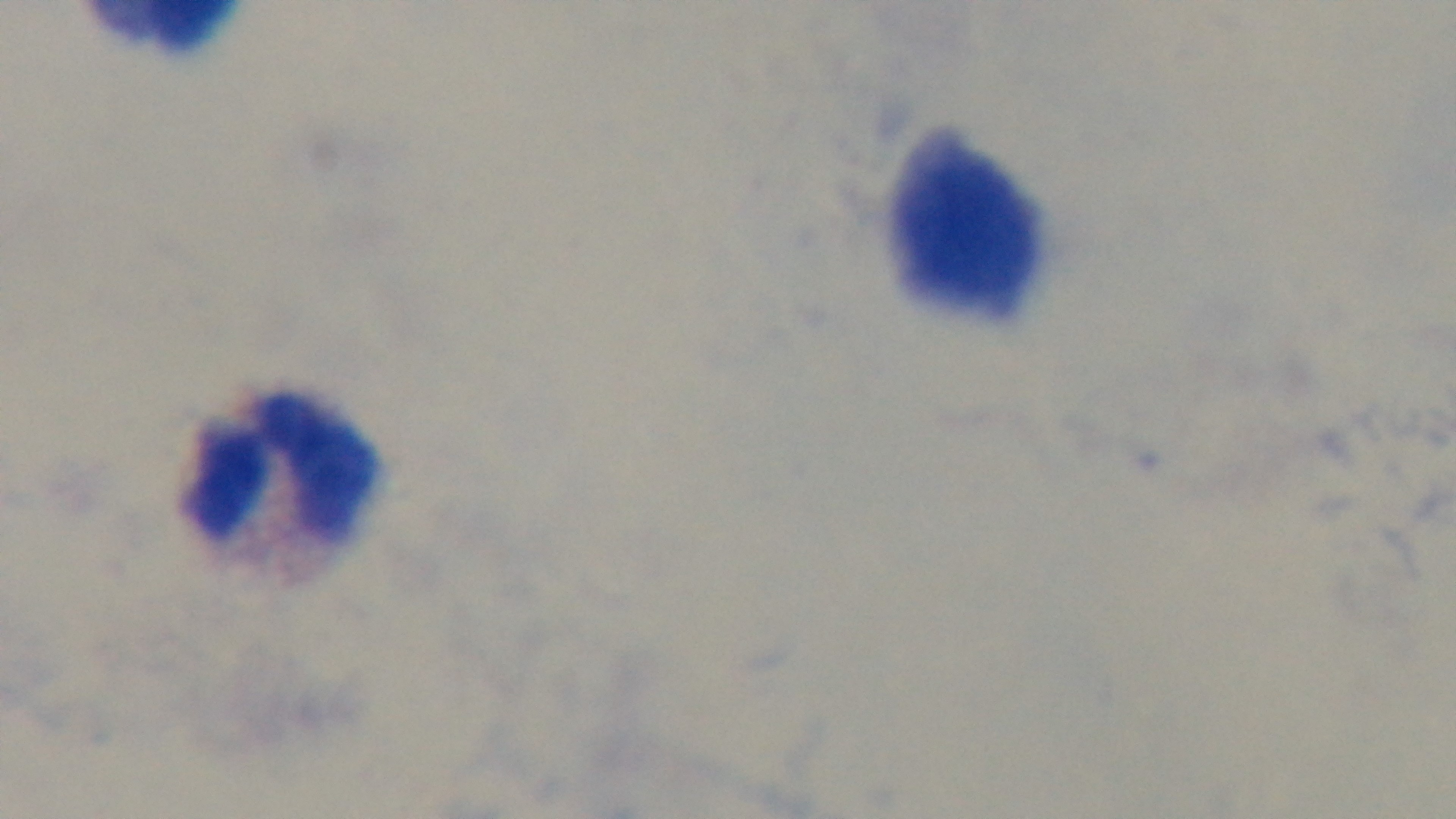

{
  "field_of_view": "single",
  "capture": "mounted 4K digital camera",
  "objective": "100x oil immersion",
  "stain": "Giemsa",
  "modality": "light microscopy",
  "preparation": "thick blood film",
  "malaria_status": "negative"
}